Locate every uninfected red blood cell.
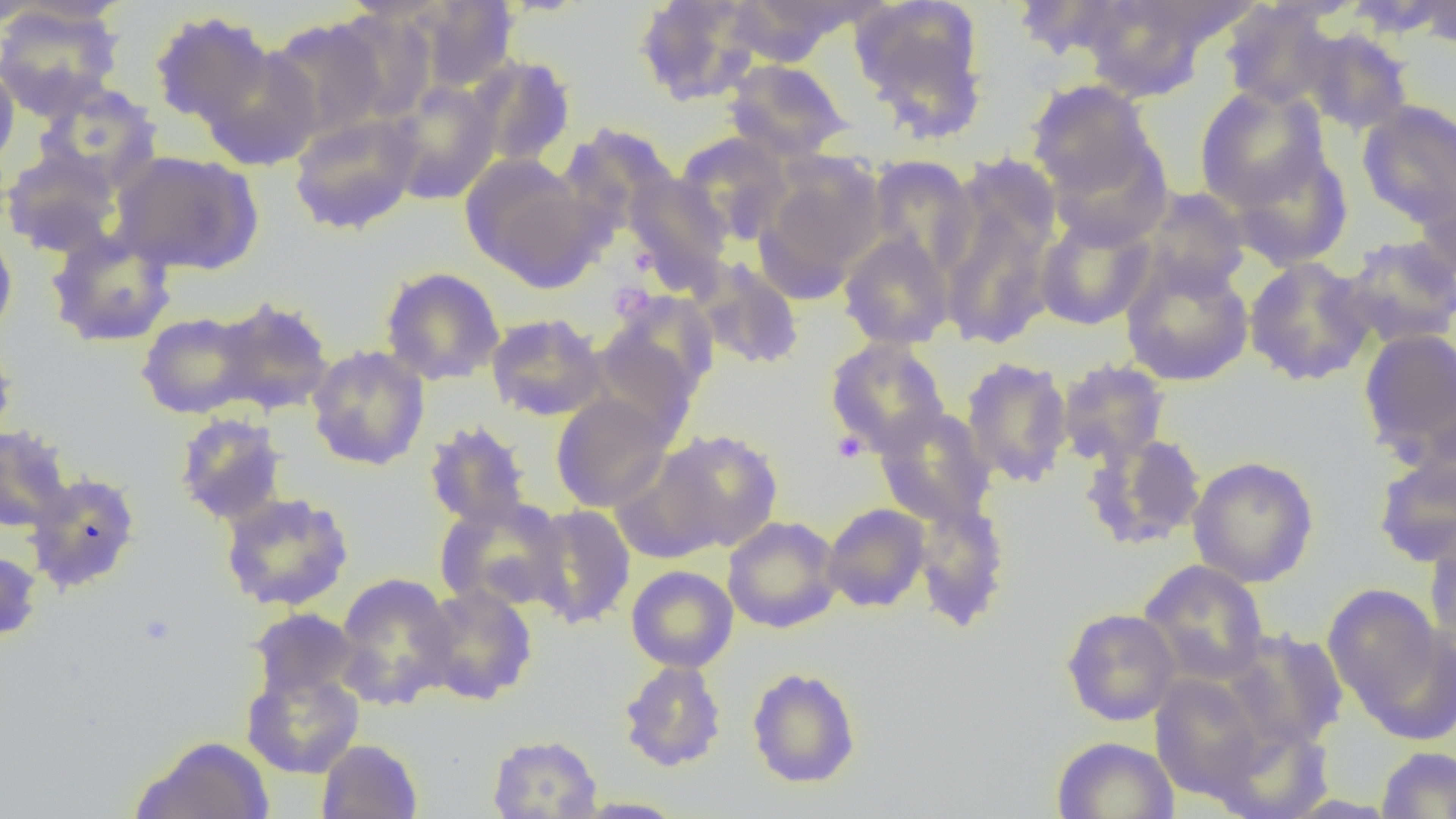

Approximate bounding boxes as named x1/y1/x2/y2 corners in pixels.
Uninfected red blood cells: (x1=0, y1=0, x2=54, y2=28), (x1=407, y1=0, x2=521, y2=94), (x1=633, y1=0, x2=764, y2=106), (x1=850, y1=0, x2=989, y2=141), (x1=1067, y1=0, x2=1233, y2=101), (x1=1408, y1=0, x2=1456, y2=51), (x1=729, y1=1, x2=882, y2=58), (x1=1011, y1=1, x2=1141, y2=61), (x1=1217, y1=2, x2=1341, y2=110), (x1=0, y1=3, x2=124, y2=119), (x1=149, y1=11, x2=276, y2=130), (x1=265, y1=18, x2=389, y2=140), (x1=1296, y1=26, x2=1415, y2=136), (x1=199, y1=45, x2=323, y2=170), (x1=469, y1=55, x2=577, y2=167), (x1=723, y1=58, x2=852, y2=161), (x1=0, y1=61, x2=20, y2=174), (x1=1026, y1=79, x2=1159, y2=202), (x1=385, y1=81, x2=501, y2=204), (x1=36, y1=82, x2=161, y2=191), (x1=1195, y1=86, x2=1329, y2=210), (x1=1357, y1=100, x2=1456, y2=228), (x1=288, y1=112, x2=423, y2=235), (x1=676, y1=133, x2=793, y2=245), (x1=1045, y1=135, x2=1174, y2=249), (x1=1226, y1=145, x2=1354, y2=271), (x1=0, y1=148, x2=123, y2=258), (x1=110, y1=150, x2=263, y2=276), (x1=459, y1=154, x2=599, y2=287), (x1=865, y1=156, x2=977, y2=277), (x1=756, y1=161, x2=885, y2=298), (x1=936, y1=168, x2=1061, y2=350), (x1=625, y1=171, x2=734, y2=287), (x1=1138, y1=187, x2=1250, y2=298), (x1=1034, y1=214, x2=1156, y2=330), (x1=0, y1=224, x2=18, y2=340), (x1=45, y1=228, x2=177, y2=348), (x1=838, y1=231, x2=954, y2=350), (x1=1337, y1=235, x2=1456, y2=348), (x1=1120, y1=255, x2=1254, y2=386), (x1=1243, y1=256, x2=1376, y2=387), (x1=693, y1=258, x2=804, y2=371), (x1=380, y1=267, x2=505, y2=386), (x1=208, y1=297, x2=335, y2=416), (x1=590, y1=302, x2=714, y2=435), (x1=136, y1=311, x2=260, y2=419), (x1=485, y1=313, x2=607, y2=421), (x1=1358, y1=327, x2=1456, y2=463), (x1=0, y1=332, x2=18, y2=448), (x1=825, y1=338, x2=950, y2=456), (x1=306, y1=345, x2=430, y2=470), (x1=960, y1=356, x2=1074, y2=488), (x1=1056, y1=359, x2=1171, y2=467), (x1=551, y1=394, x2=673, y2=512), (x1=874, y1=405, x2=997, y2=528), (x1=174, y1=412, x2=288, y2=526), (x1=423, y1=420, x2=533, y2=531), (x1=0, y1=424, x2=74, y2=533), (x1=654, y1=429, x2=783, y2=552), (x1=1081, y1=432, x2=1208, y2=550), (x1=1373, y1=451, x2=1456, y2=568), (x1=1187, y1=455, x2=1319, y2=588), (x1=25, y1=472, x2=141, y2=594), (x1=219, y1=492, x2=354, y2=612), (x1=911, y1=495, x2=1012, y2=631), (x1=435, y1=496, x2=569, y2=613), (x1=822, y1=503, x2=931, y2=613), (x1=526, y1=504, x2=637, y2=629), (x1=723, y1=515, x2=843, y2=634), (x1=1424, y1=523, x2=1456, y2=652), (x1=0, y1=548, x2=43, y2=644), (x1=1138, y1=559, x2=1270, y2=685), (x1=626, y1=565, x2=739, y2=672), (x1=333, y1=572, x2=460, y2=710), (x1=1322, y1=582, x2=1449, y2=729), (x1=416, y1=584, x2=538, y2=704), (x1=1061, y1=607, x2=1182, y2=726), (x1=247, y1=608, x2=363, y2=703), (x1=1223, y1=628, x2=1349, y2=751), (x1=618, y1=660, x2=727, y2=772), (x1=747, y1=667, x2=861, y2=788), (x1=241, y1=668, x2=365, y2=778), (x1=1150, y1=673, x2=1271, y2=801), (x1=1210, y1=719, x2=1335, y2=819), (x1=487, y1=733, x2=602, y2=818), (x1=131, y1=735, x2=274, y2=818), (x1=1051, y1=735, x2=1179, y2=819), (x1=316, y1=739, x2=423, y2=819), (x1=1376, y1=746, x2=1456, y2=818), (x1=572, y1=796, x2=689, y2=818).

Summary:
  - Platelet locations: (x1=608, y1=281, x2=657, y2=325), (x1=832, y1=430, x2=868, y2=463)
  - Slide-level diagnosis: negative for blood parasites
  - Magnification: 1000x
  - Field of view: single
  - Modality: light microscopy
  - Image size: 1456×819 pixels
  - Preparation: thin blood film